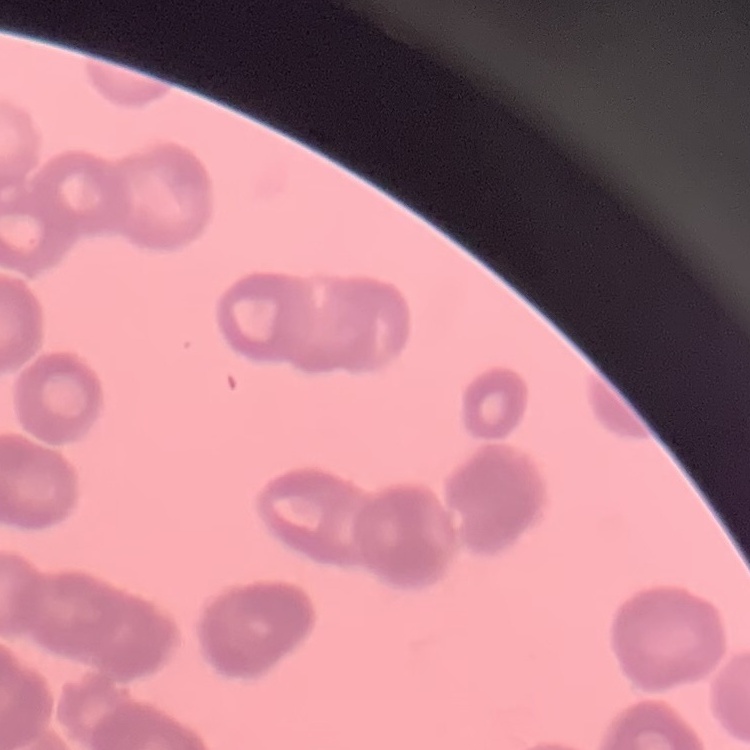 The red blood cells show rouleaux formation. Field's or Giemsa stain. Thin peripheral smear. Square crop of a larger photomicrograph.